State which parasite is depicted.
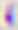
This is Toxoplasma gondii.

Micrograph. Captured at 400x magnification.